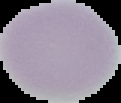 Cell region segmented out of the field of view; the surrounding area is masked to black. From a thin blood film. Image is 121×103 pixels. Malaria status: uninfected.